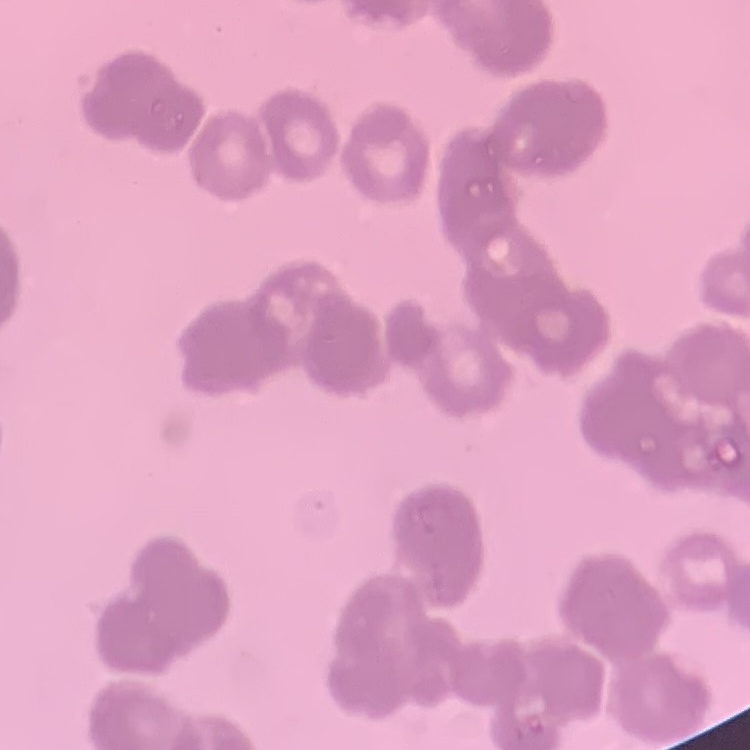

Summary:
  - Red blood cell morphology: rouleaux formation
  - Image type: one tile cut from a larger photomicrograph
  - Preparation: thin blood smear
  - Stain: Field's or Giemsa